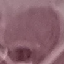

Summary:
  - Malaria status: uninfected
  - Capture: smartphone through the microscope eyepiece
  - Preparation: thin blood smear
  - Stain: Giemsa
  - Image type: cell patch, automatically extracted from a larger field of view and resized to 64 × 64 pixels